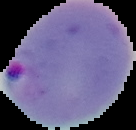
From a thin blood smear. Image is 136×130 pixels. The area outside the segmented cell region is set to black. Result: malaria parasites identified.